Identify the blood parasite species.
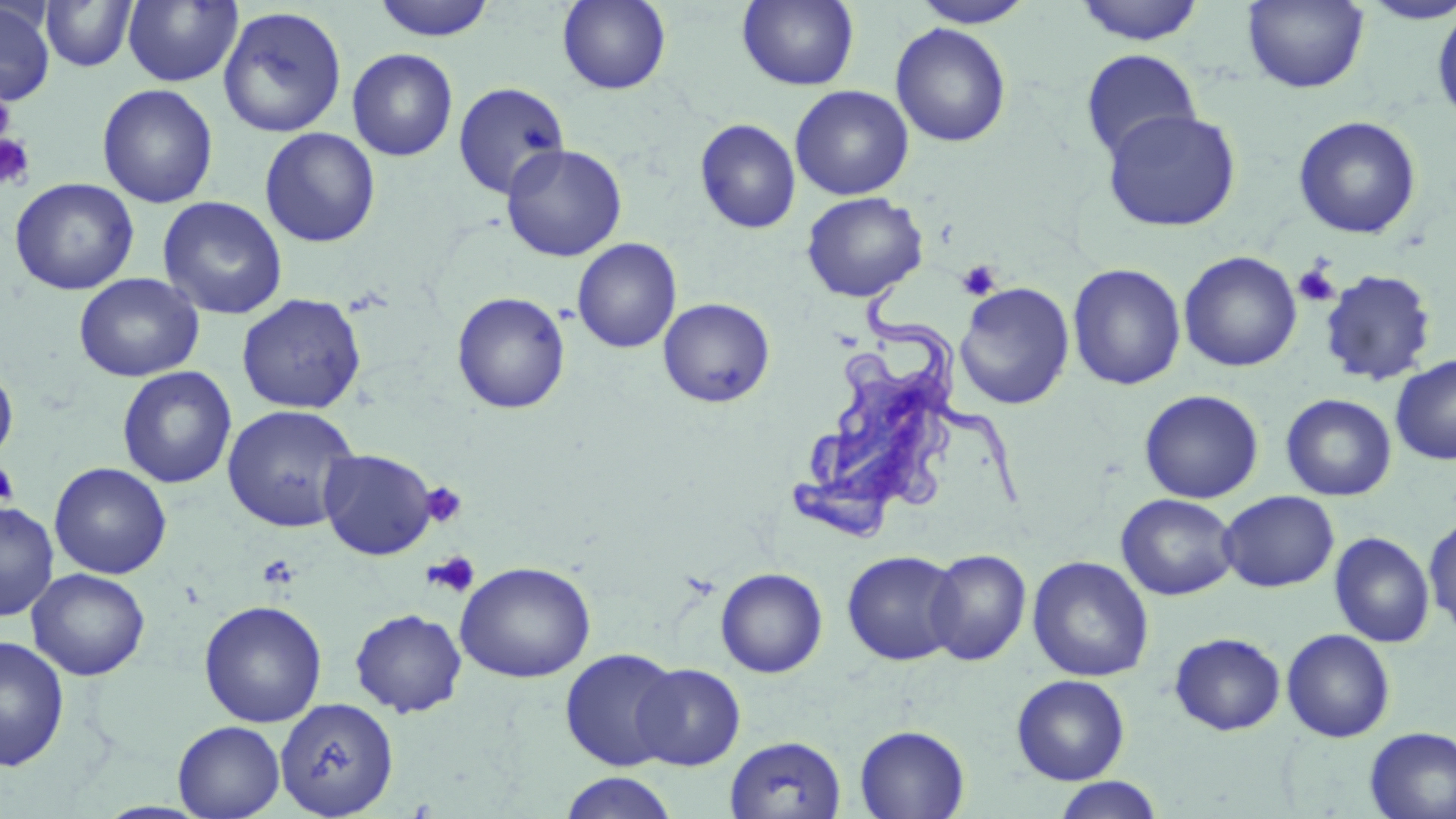
Trypanosoma brucei.

uninfected red blood cell locations = approximate bounding boxes as (x1,y1)-(x2,y2) corner pairs in pixels: (122,0)-(243,88), (371,0)-(497,42), (557,0)-(671,94), (737,0)-(859,91), (909,0)-(1036,28), (1242,0)-(1369,93), (1354,0)-(1456,25), (40,1)-(139,72), (1074,1)-(1205,46), (0,2)-(56,107), (117,3)-(237,185), (1431,5)-(1456,127), (217,6)-(348,138), (890,23)-(1011,148), (347,48)-(459,161), (1080,48)-(1202,162), (452,81)-(570,200), (97,83)-(218,208), (790,85)-(914,200), (1101,108)-(1242,232), (1293,115)-(1422,239), (695,118)-(801,234), (260,127)-(381,248), (501,143)-(627,262), (9,178)-(139,296), (801,192)-(928,302), (157,196)-(288,320), (572,238)-(682,353), (1178,251)-(1302,372), (1067,263)-(1186,391), (1318,270)-(1437,387), (73,273)-(204,382), (955,282)-(1075,410), (452,292)-(571,414), (237,294)-(366,414), (658,297)-(775,408), (1390,354)-(1456,465), (0,361)-(18,465), (117,366)-(236,489), (1138,389)-(1264,504), (1281,393)-(1396,501), (221,404)-(360,533), (318,449)-(437,560), (49,462)-(172,579), (1218,490)-(1340,593), (1116,493)-(1239,601), (0,501)-(59,622), (1424,515)-(1456,635), (1329,531)-(1435,648), (925,549)-(1032,666), (842,550)-(962,666), (1027,556)-(1154,682), (455,561)-(595,683), (716,563)-(963,670), (715,567)-(828,678), (27,568)-(150,681), (199,600)-(327,727), (350,609)-(467,717), (1281,629)-(1395,742), (1169,632)-(1286,735), (0,634)-(70,772), (559,648)-(683,771), (632,663)-(746,770), (1011,674)-(1130,784), (275,697)-(399,817), (173,720)-(285,818), (854,724)-(970,819), (1364,726)-(1456,818), (725,735)-(847,819), (559,772)-(679,819), (1052,777)-(1165,819)
Trypanosoma brucei locations = approximate bounding boxes as (x1,y1)-(x2,y2) corner pairs in pixels: (786,279)-(1047,546)
preparation = thin blood smear
stain = May-Grünwald-Giemsa
platelet locations = approximate bounding boxes as (x1,y1)-(x2,y2) corner pairs in pixels: (0,88)-(15,146), (0,133)-(36,191), (956,259)-(1002,301), (1293,264)-(1340,307), (0,460)-(18,508), (421,481)-(468,528), (423,550)-(481,598), (258,554)-(300,589)
magnification = 1000x
image size = 1456×819 pixels
modality = light microscopy
field of view = one of a larger specimen